Comment on the morphology of the erythrocytes.
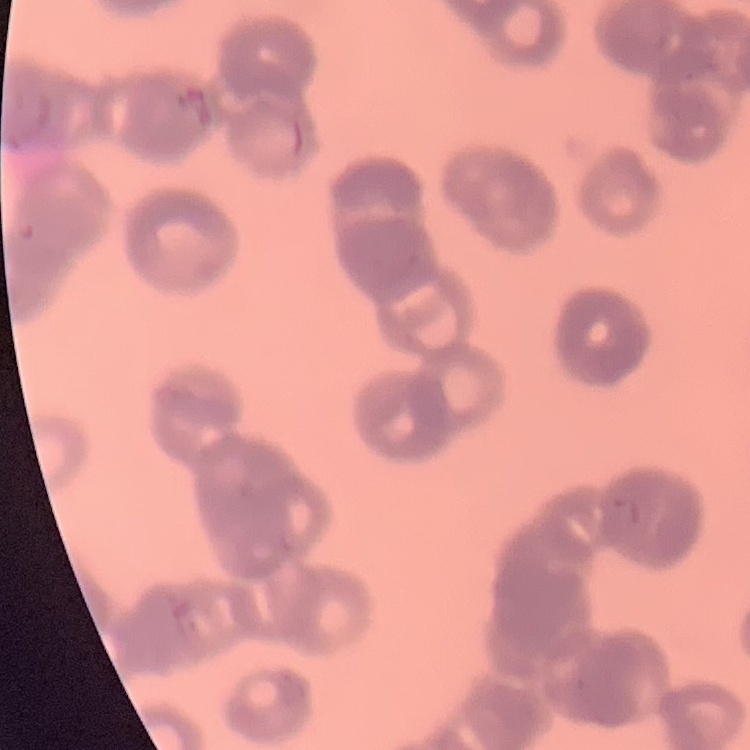
They show rouleaux formation.

One tile cut from a larger photomicrograph. Field's or Giemsa stain. Thin peripheral smear.